Classify this cell by malaria status.
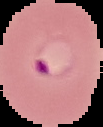
It is parasitized.

Summary:
  - Image size: 103×127 pixels
  - Preparation: thin blood film
  - Image type: segmented cell region on a black background